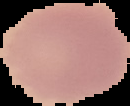
image_type: cell region segmented out of the field of view; surrounding area masked to black
preparation: thin blood smear
image_size: 130×106 pixels
malaria_status: uninfected